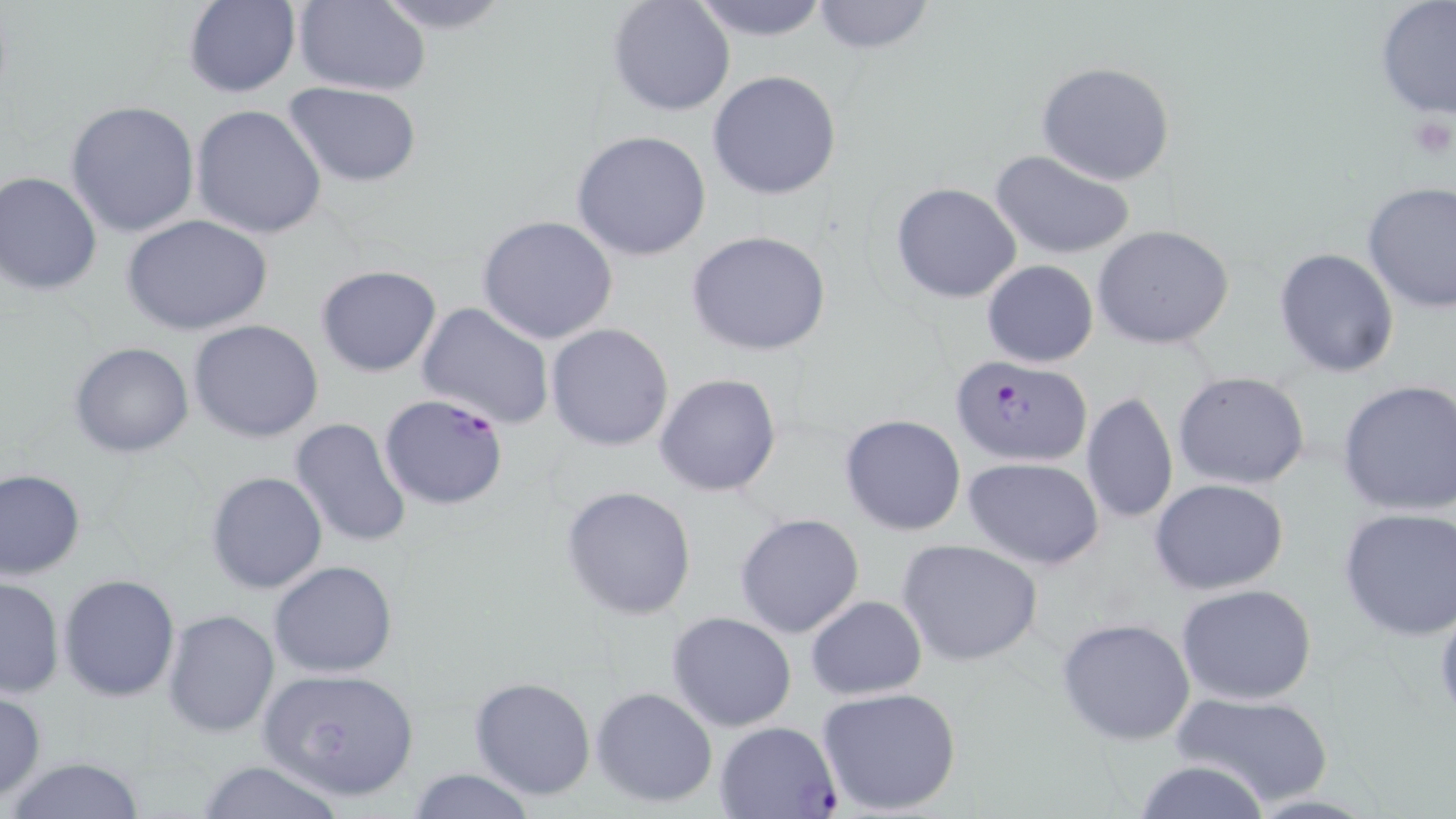 Approximate bounding boxes as (x1,y1)-(x2,y2) corner pairs in pixels. Plasmodium falciparum-infected red blood cell locations: (956,354)-(1093,465), (378,393)-(509,510), (716,720)-(840,817). Uninfected red blood cell locations: (367,0)-(517,33), (608,0)-(735,118), (687,0)-(834,40), (810,0)-(935,53), (1373,0)-(1456,124), (182,1)-(301,99), (292,1)-(431,95), (1037,61)-(1177,186), (706,70)-(842,199), (285,82)-(422,186), (66,99)-(201,238), (190,104)-(328,240), (571,131)-(712,261), (989,148)-(1136,262), (0,171)-(102,296), (1361,181)-(1456,313), (890,183)-(1022,301), (124,215)-(273,335), (477,215)-(619,344), (1093,225)-(1237,350), (687,231)-(832,357), (1273,248)-(1399,377), (981,260)-(1099,367), (316,265)-(441,377), (416,302)-(554,429), (189,319)-(324,442), (546,323)-(674,450), (69,342)-(195,458), (1172,371)-(1311,492), (654,372)-(782,498), (1337,379)-(1456,516), (1080,390)-(1179,526), (839,414)-(967,537), (290,417)-(412,548), (964,458)-(1105,570), (1,469)-(85,579), (205,472)-(328,593), (1150,478)-(1289,596), (560,485)-(698,619), (1339,505)-(1456,640), (734,512)-(865,639), (897,538)-(1044,667), (269,561)-(398,678), (59,574)-(180,702), (0,576)-(65,700), (1175,583)-(1319,703), (806,595)-(927,700), (1432,597)-(1456,723), (162,608)-(280,737), (667,611)-(798,732), (1057,617)-(1196,746), (258,667)-(420,801), (469,676)-(596,801), (815,685)-(963,816), (590,686)-(718,808), (0,689)-(46,800), (1171,691)-(1335,806), (5,756)-(148,819), (193,759)-(349,819), (1131,759)-(1272,819), (404,768)-(540,819), (1237,792)-(1384,817). Slide-level diagnosis: Plasmodium falciparum. May-Grünwald-Giemsa-stained preparation. Optical microscopy. Thin blood smear. Single field of view. Image is 1456×819 pixels. 1000x magnification.